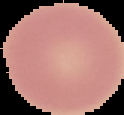
Cell region segmented out of the field of view; the surrounding area is masked to black. Image is 124×115 pixels. Malaria status: uninfected. From a thin blood film.